Classify this cell by malaria status.
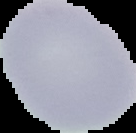

Uninfected.

Summary:
  - Image type: segmented cell region with the area outside set to black
  - Image size: 136×133 pixels
  - Preparation: thin blood film